Locate and identify every blood parasite.
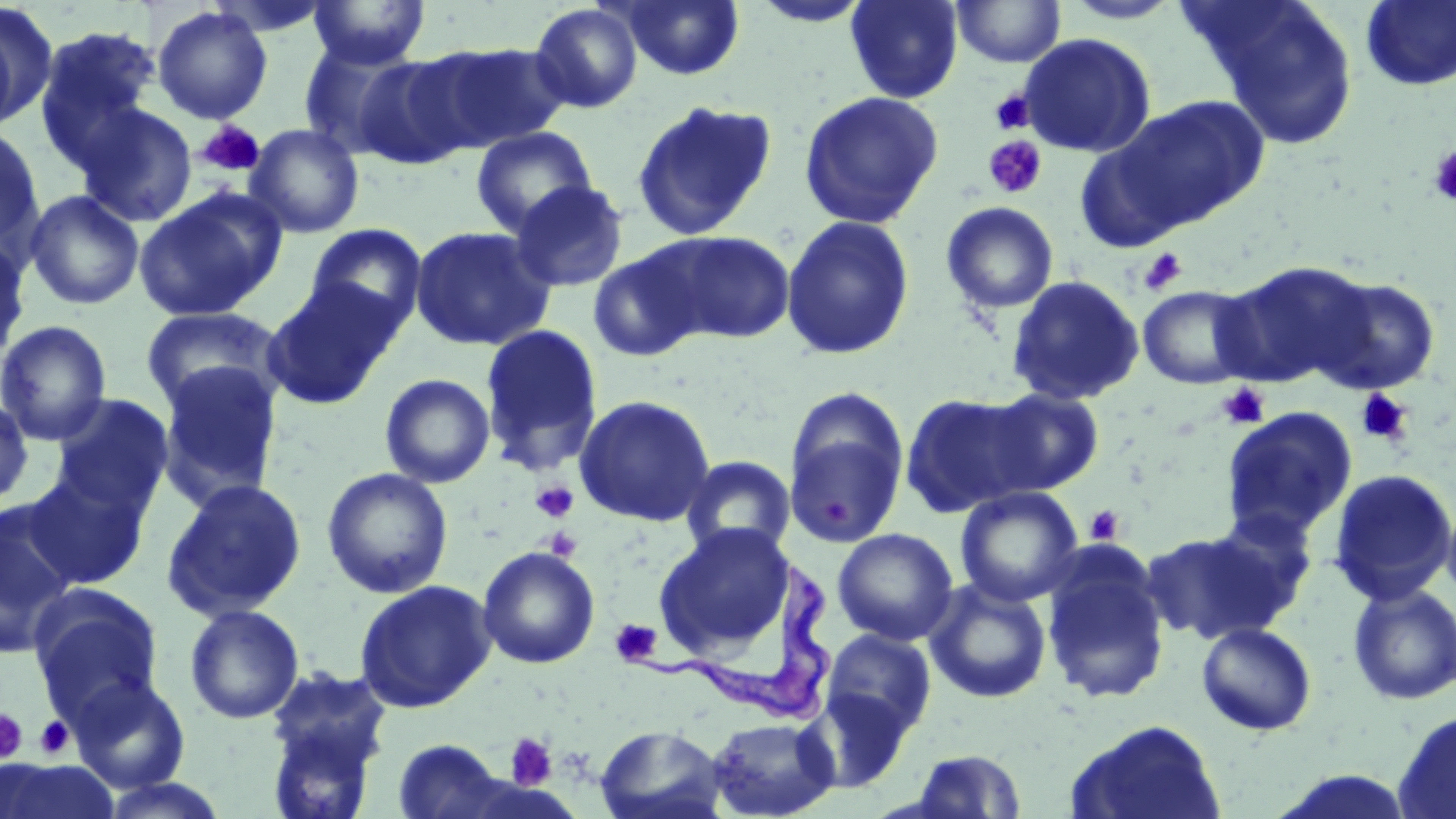
Approximate bounding boxes as (x1, y1, x2, y2) in pixels.
Trypanosoma brucei: (635, 563, 834, 724).
No Plasmodium falciparum, Plasmodium ovale, Plasmodium malariae, Plasmodium vivax, or Babesia divergens observed.

Platelet locations: (990, 89, 1035, 134), (197, 119, 265, 178), (983, 136, 1047, 199), (1426, 145, 1456, 206), (1139, 248, 1188, 296), (1217, 383, 1270, 430), (1354, 389, 1413, 446), (531, 480, 579, 523), (825, 498, 853, 528), (1084, 506, 1125, 546), (543, 527, 582, 561), (609, 618, 663, 667), (0, 708, 29, 764), (33, 715, 76, 760), (504, 732, 558, 791). Uninfected red blood cell locations: (307, 0, 431, 69), (620, 0, 744, 80), (749, 0, 873, 28), (845, 0, 963, 103), (1060, 0, 1184, 24), (1189, 0, 1361, 148), (950, 1, 1066, 69), (1360, 1, 1456, 91), (1, 3, 55, 131), (529, 3, 643, 113), (152, 6, 273, 124), (0, 15, 23, 136), (33, 25, 162, 168), (1019, 33, 1156, 157), (298, 39, 420, 159), (416, 42, 569, 153), (352, 55, 473, 169), (798, 91, 944, 229), (1108, 95, 1271, 232), (631, 100, 777, 241), (76, 103, 198, 227), (244, 124, 365, 238), (0, 126, 45, 254), (470, 126, 597, 237), (509, 180, 629, 293), (134, 189, 285, 322), (25, 190, 145, 310), (941, 201, 1059, 314), (780, 214, 915, 360), (305, 223, 427, 332), (409, 225, 556, 351), (649, 229, 797, 344), (0, 232, 31, 367), (587, 247, 707, 363), (1214, 259, 1374, 388), (1310, 274, 1443, 395), (1006, 275, 1145, 406), (263, 279, 401, 409), (1137, 285, 1259, 390), (140, 305, 286, 414), (0, 320, 113, 445), (479, 324, 603, 474), (155, 361, 283, 508), (380, 373, 495, 488), (983, 387, 1105, 494), (900, 392, 1037, 518), (50, 393, 173, 515), (574, 394, 716, 527), (0, 398, 34, 507), (1220, 406, 1358, 543), (784, 408, 908, 549), (680, 455, 797, 558), (321, 467, 454, 599), (1327, 468, 1456, 606), (21, 470, 152, 590), (161, 479, 307, 622), (955, 486, 1084, 607), (1441, 494, 1456, 609), (0, 502, 80, 658), (1201, 508, 1318, 629), (653, 522, 794, 660), (1142, 527, 1296, 646), (832, 528, 959, 646), (477, 546, 600, 669), (1040, 547, 1171, 704), (354, 579, 498, 713), (923, 579, 1052, 704), (1347, 583, 1456, 706), (28, 584, 164, 722), (184, 604, 305, 725), (1196, 621, 1317, 736), (821, 629, 937, 740), (264, 667, 392, 811), (68, 674, 191, 792), (803, 689, 913, 793), (1392, 709, 1456, 819), (707, 716, 838, 819), (1065, 718, 1227, 818), (595, 724, 728, 819), (392, 738, 511, 819), (908, 748, 1027, 818), (0, 758, 119, 819), (1265, 769, 1421, 818). Slide-level diagnosis: Trypanosoma brucei. May-Grünwald-Giemsa-stained preparation. Image is 1456×819 pixels. 1000x magnification. Thin blood smear. Light microscopy. One field of a larger specimen.